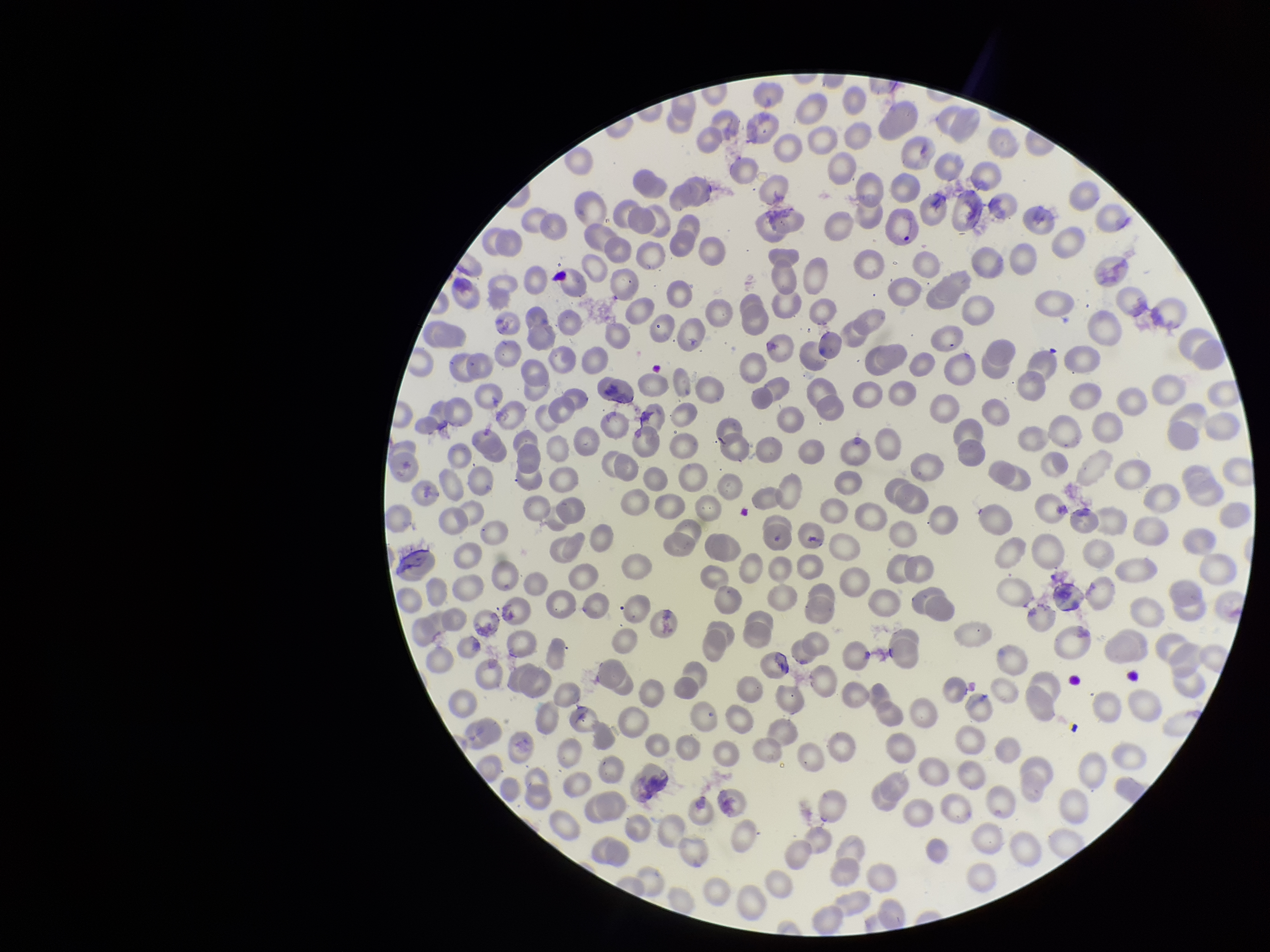
field of view = single
species reported for this patient = Plasmodium vivax
capture = smartphone photograph through the microscope eyepiece
patient malaria status = positive
stain = Giemsa
parasitized red blood cell count = 0
red blood cell count = 292
image size = 1270×952 pixels
parasitized red blood cells = none identified
preparation = thin